Identify the preparation type.
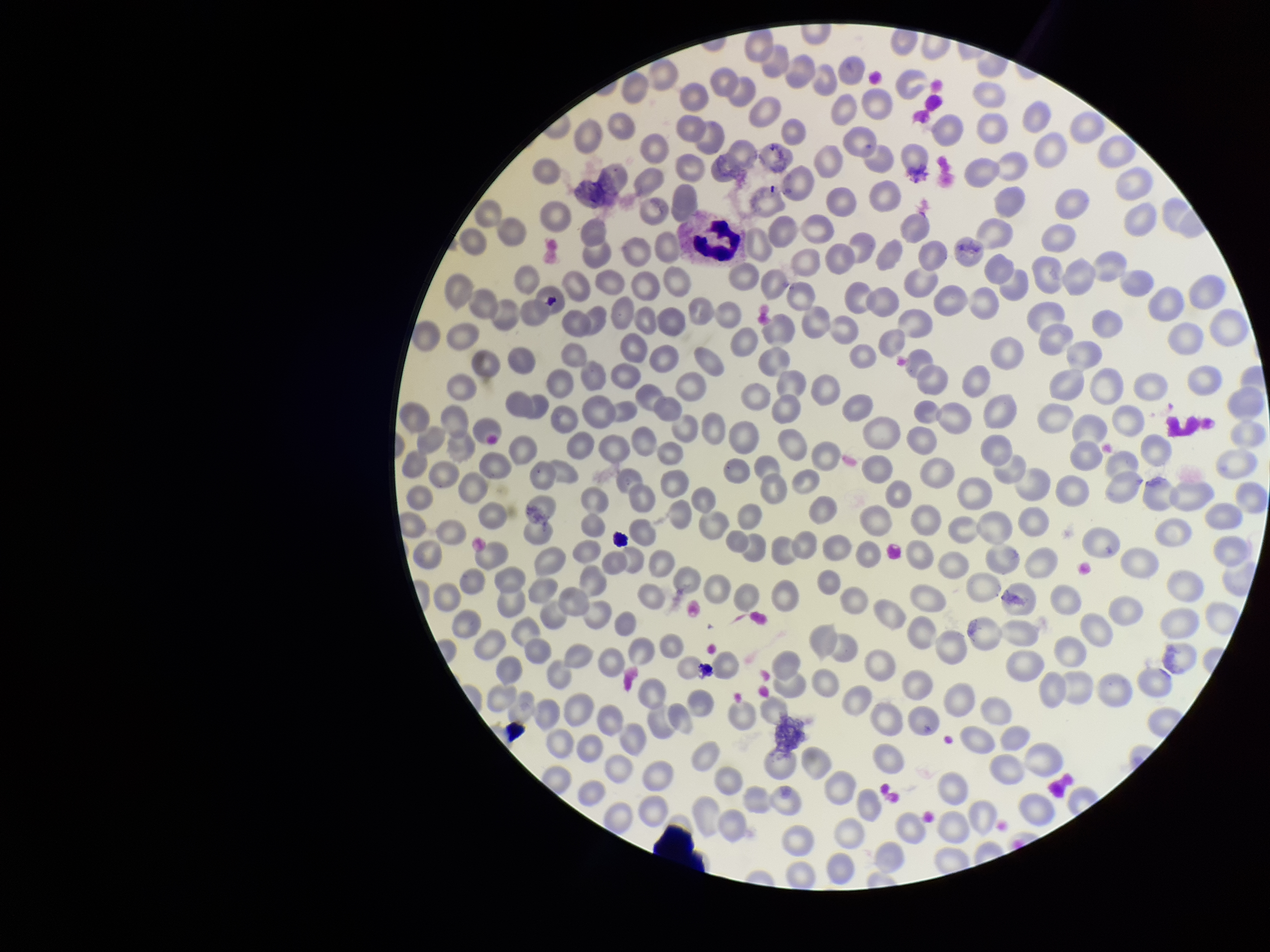

A thin smear.

Photographed through the microscope eyepiece with a smartphone camera. Image is 1270×952 pixels. One field from this slide. Stained with Giemsa. Red blood cell count: 273. Patient malaria status: negative. Parasitized red blood cells: none identified. Parasitized red blood cell count: 0.